Locate Plasmodium parasites and leukocytes.
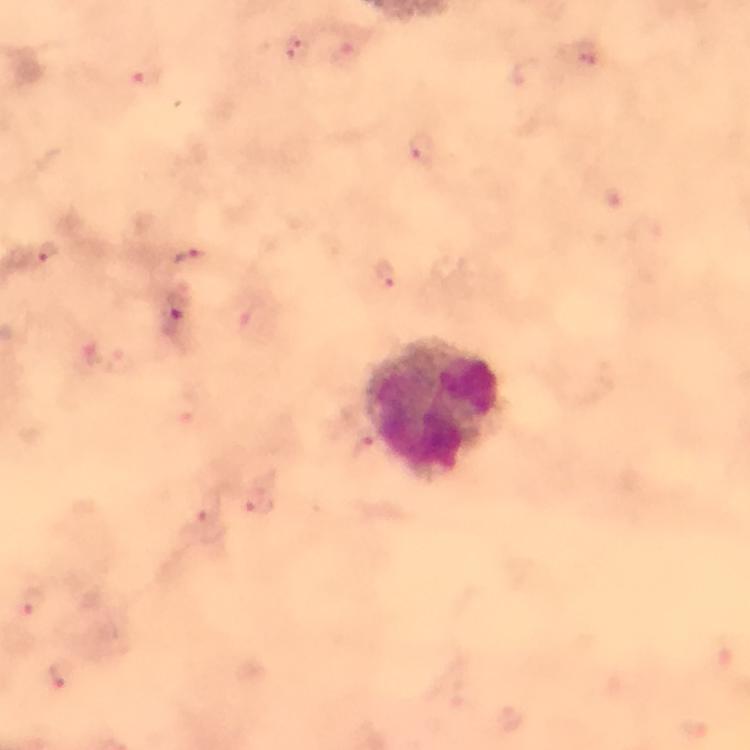

Approximate centers as [x, y] in pixels.
Plasmodium parasites: [297, 50], [421, 150], [44, 253], [190, 257], [385, 276], [174, 316], [258, 503], [209, 508], [33, 602], [59, 673].
Leukocytes: [436, 407].

Image is 750×750 pixels. Cropped region of a single field of view. Thick blood film. Photographed with a smartphone mounted on the microscope. Immersion oil was used. From a diagnostic examination for malaria. Giemsa stain. At 100x magnification.